Report the malaria status of this cell.
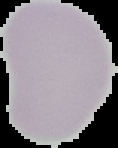
It is uninfected.

Image is 118×148 pixels. Segmented cell region on a black background. From a thin blood film.